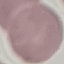

Result: negative for malaria parasites. Giemsa stain. Automatically extracted cell patch, resized to 64 × 64 pixels. Photographed with a smartphone camera at the microscope eyepiece. Thin blood film.